Locate every Plasmodium parasite.
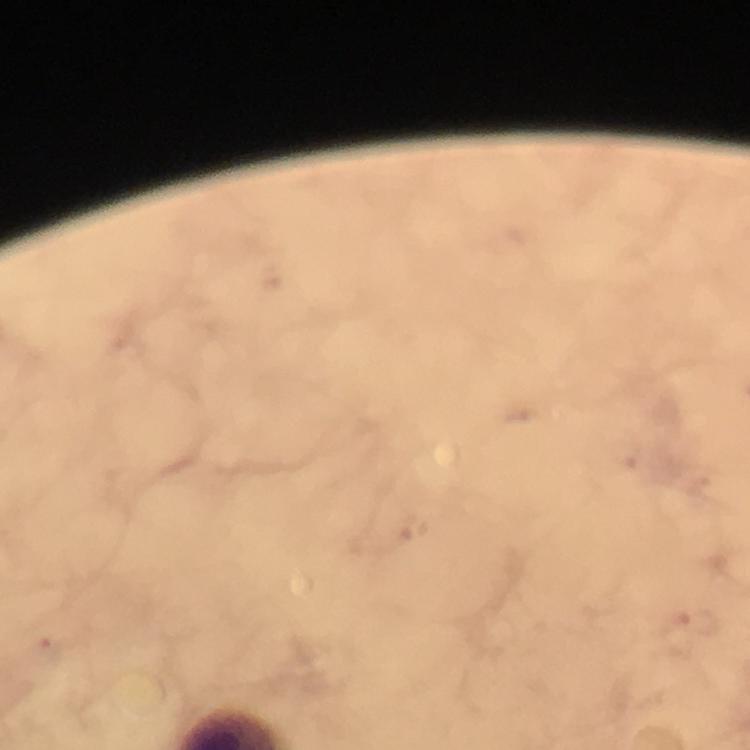

Approximate centers as [x, y] in pixels.
Plasmodium parasites: [413, 527], [699, 623], [46, 650].

Thick blood smear. Photographed with a smartphone mounted on the microscope. Giemsa stain. At 100x magnification. A crop from one field of view. Image is 750×750 pixels. From a diagnostic examination for malaria. Immersion oil applied.